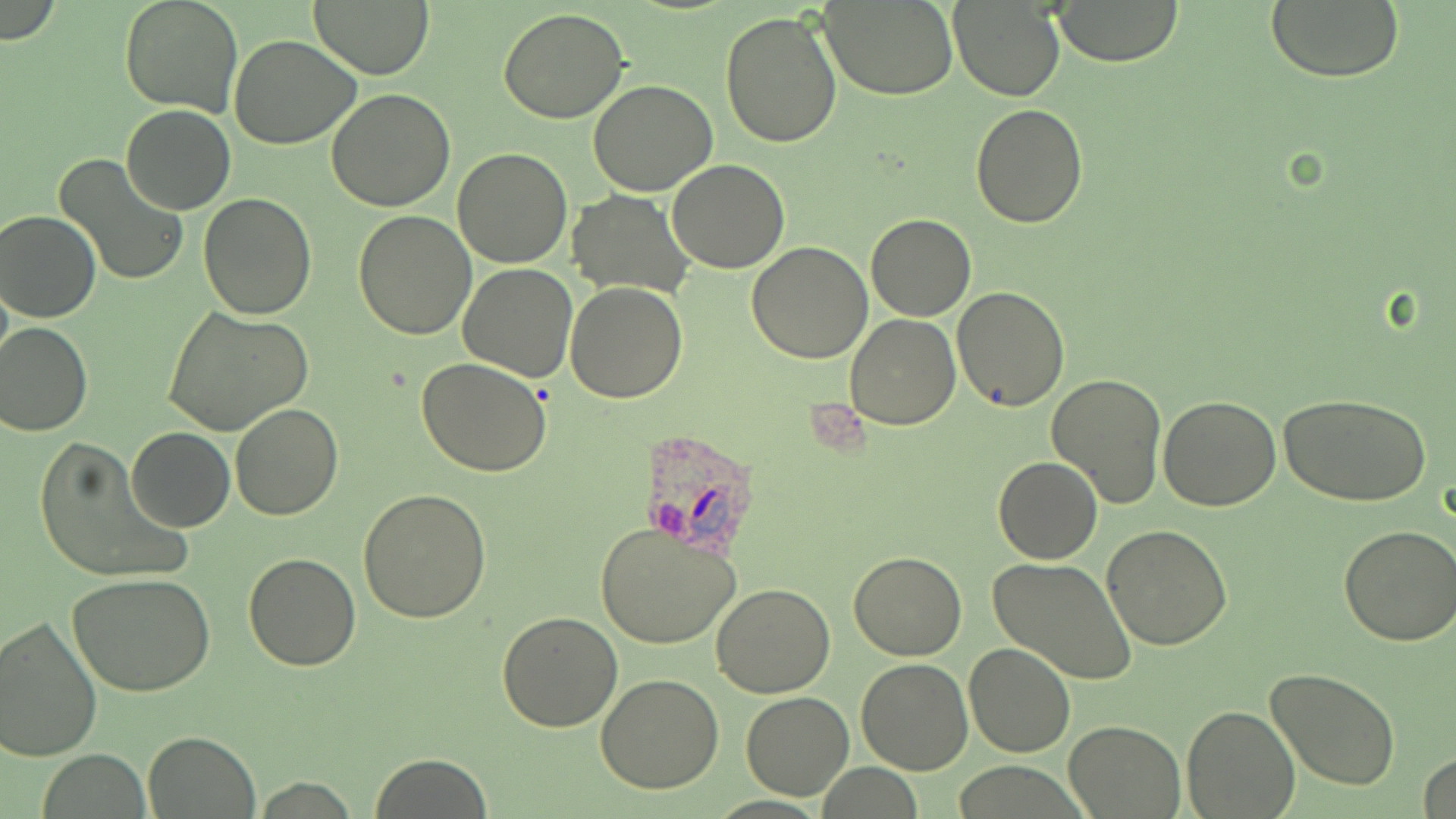
Approximate bounding boxes as [x1, y1, x2, y2] in pixels. Plasmodium ovale-infected red blood cell locations: [645, 436, 770, 565]. Uninfected red blood cell locations: [118, 0, 243, 116], [310, 0, 434, 79], [1265, 0, 1405, 83], [822, 2, 957, 99], [949, 2, 1064, 102], [1054, 2, 1182, 66], [498, 7, 630, 124], [720, 10, 842, 149], [229, 35, 362, 149], [587, 79, 717, 196], [326, 88, 455, 211], [971, 103, 1088, 228], [121, 104, 235, 214], [452, 147, 573, 268], [54, 152, 188, 287], [666, 159, 791, 273], [569, 189, 692, 297], [200, 192, 317, 319], [0, 210, 101, 323], [352, 210, 476, 340], [867, 214, 976, 322], [747, 242, 874, 365], [458, 264, 579, 382], [565, 283, 688, 403], [952, 285, 1070, 411], [162, 306, 314, 437], [845, 313, 960, 430], [0, 323, 93, 437], [416, 357, 552, 476], [1046, 372, 1168, 509], [1279, 392, 1435, 510], [1158, 395, 1282, 511], [231, 401, 343, 520], [125, 426, 234, 531], [32, 437, 188, 583], [993, 456, 1101, 564], [358, 489, 491, 623], [594, 519, 742, 648], [1102, 524, 1233, 649], [1339, 526, 1455, 646], [846, 551, 966, 660], [243, 553, 361, 671], [988, 557, 1139, 687], [68, 572, 216, 699], [710, 581, 837, 698], [496, 610, 622, 731], [0, 614, 103, 762], [964, 642, 1075, 758], [856, 657, 973, 775], [1266, 667, 1401, 791], [596, 674, 725, 793], [740, 691, 854, 800], [1184, 705, 1299, 818], [1063, 720, 1184, 817], [144, 731, 259, 817], [369, 752, 493, 818], [1416, 752, 1456, 819]. Slide-level diagnosis: Plasmodium ovale. Image is 1456×819 pixels. May-Grünwald-Giemsa-stained preparation. Optical microscopy. Captured at 1000x magnification. Thin blood film. One field of a larger specimen.